Evaluate for malaria.
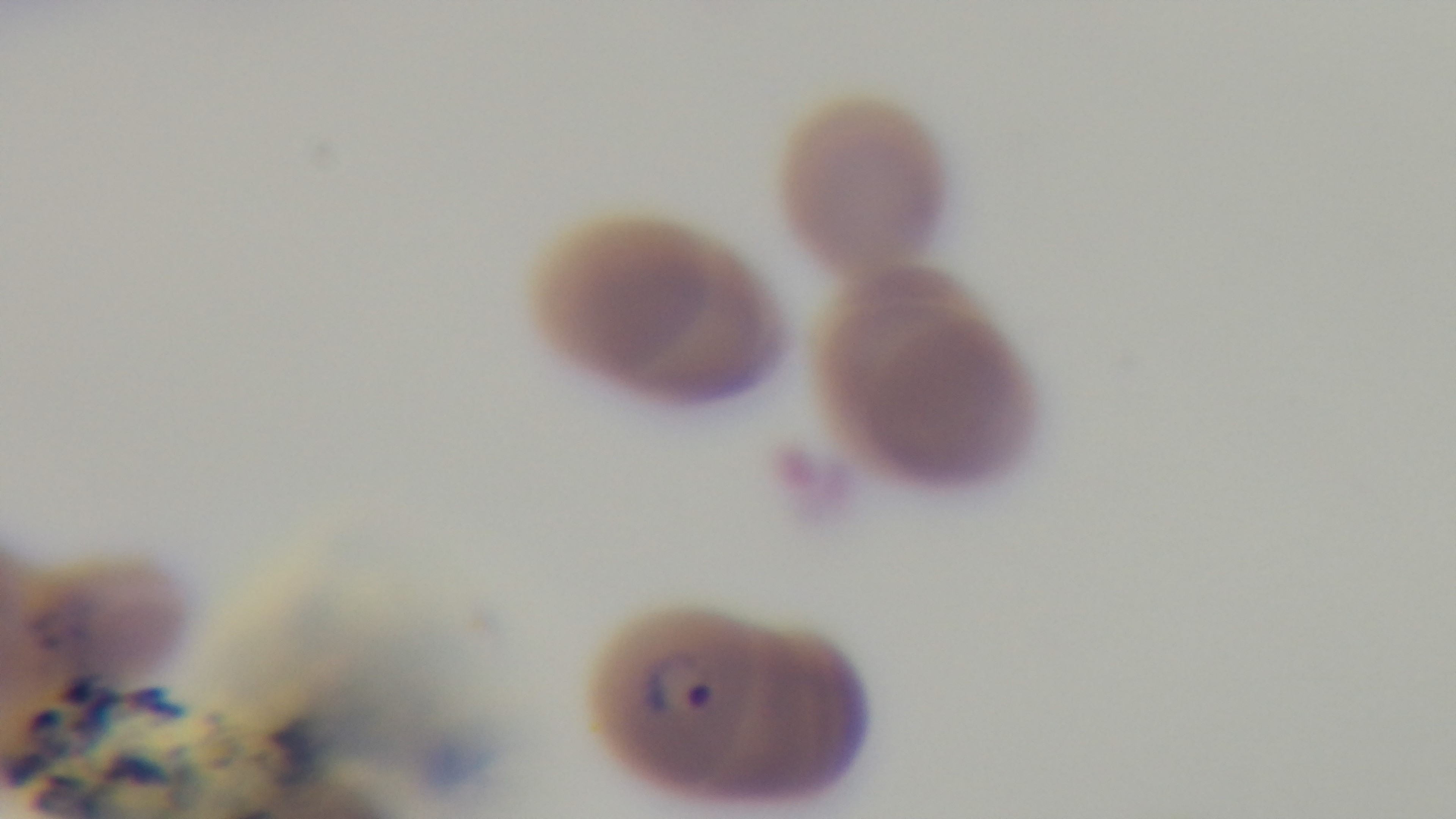
Positive.

preparation = thin smear
field of view = single
objective = 100x oil immersion
modality = light microscopy
stain = Giemsa
capture = mounted 4K digital camera